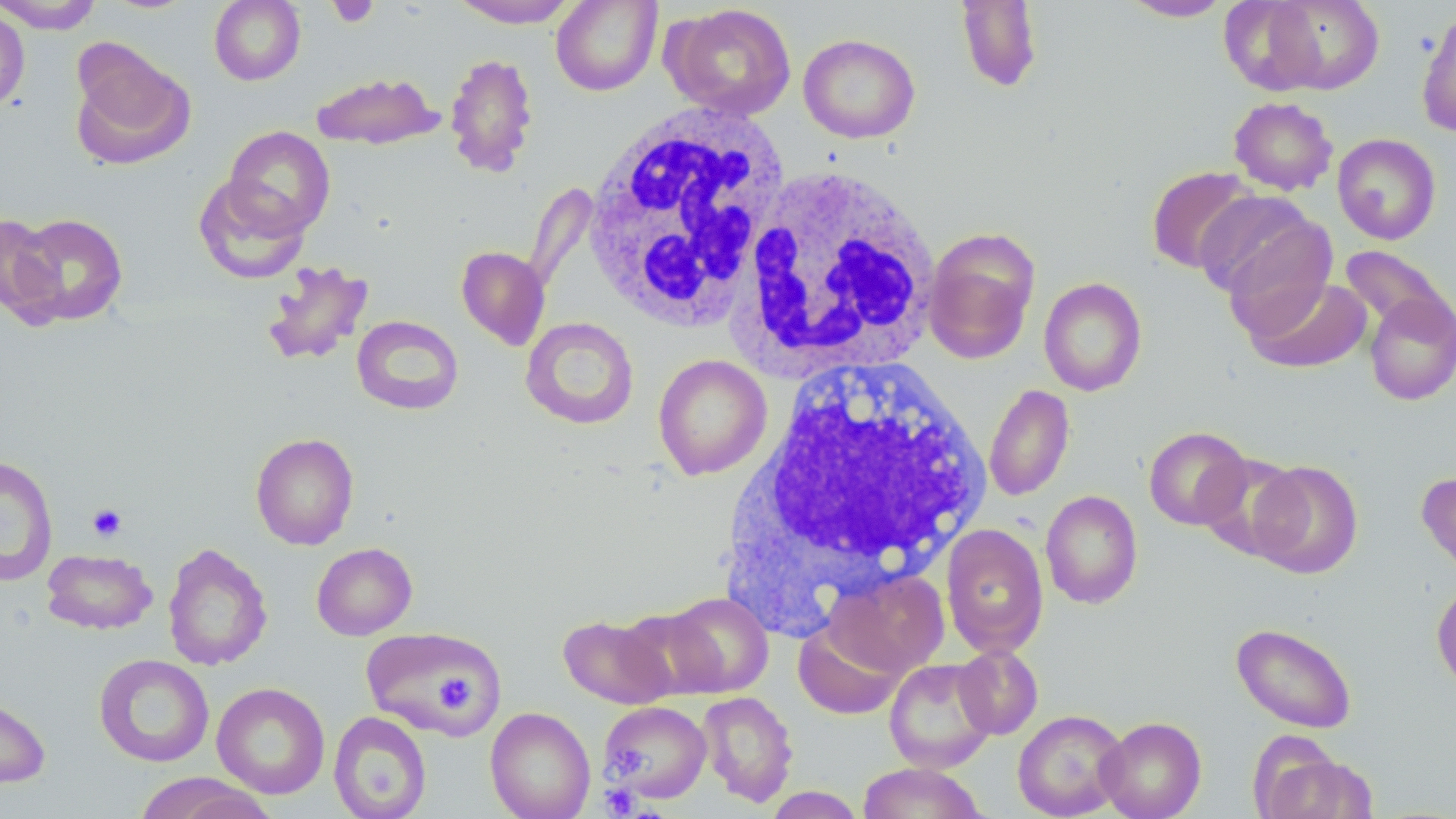
Summary:
  - Coordinate format: approximate bounding boxes as [x1, y1, x2, y2] in pixels
  - Uninfected red blood cell locations: [0, 0, 103, 34], [209, 0, 306, 86], [446, 0, 583, 28], [955, 0, 1043, 93], [1118, 0, 1234, 22], [551, 1, 662, 96], [1255, 1, 1385, 94], [6, 3, 76, 62], [664, 4, 797, 120], [0, 7, 30, 110], [1416, 10, 1456, 137], [798, 33, 921, 143], [69, 42, 194, 171], [444, 52, 539, 178], [311, 71, 443, 151], [1228, 97, 1338, 196], [224, 126, 334, 237], [1332, 133, 1441, 244], [1146, 166, 1259, 274], [194, 176, 311, 284], [1192, 190, 1327, 306], [11, 213, 129, 327], [0, 214, 65, 323], [923, 229, 1040, 364], [1338, 245, 1455, 345], [456, 246, 550, 350], [260, 259, 374, 367], [1038, 276, 1147, 397], [1245, 276, 1373, 373], [1363, 291, 1456, 406], [352, 315, 464, 415], [520, 317, 639, 430], [652, 353, 772, 480], [984, 383, 1075, 501], [1144, 426, 1252, 530], [250, 432, 359, 550], [1197, 451, 1305, 562], [0, 456, 58, 587], [1249, 460, 1364, 579], [1417, 470, 1456, 580], [1041, 489, 1143, 609], [940, 523, 1049, 657], [162, 542, 273, 671], [312, 542, 417, 640], [42, 549, 157, 634], [823, 568, 949, 677], [1432, 579, 1456, 690], [660, 592, 773, 698], [558, 612, 677, 709], [793, 620, 907, 719], [1231, 622, 1357, 734], [361, 627, 506, 736], [953, 644, 1044, 739], [94, 654, 214, 767], [883, 657, 998, 774], [212, 682, 330, 799], [698, 690, 798, 807], [0, 692, 51, 788], [600, 700, 711, 804], [485, 706, 596, 819], [1012, 709, 1129, 819], [328, 711, 432, 818], [1096, 716, 1206, 819], [1254, 745, 1377, 819], [856, 762, 988, 819], [131, 773, 277, 818], [763, 787, 866, 818]
  - Platelet locations: [327, 0, 379, 28], [87, 503, 127, 542], [434, 674, 473, 711], [612, 743, 645, 775], [601, 783, 640, 816]
  - White blood cell locations: [581, 103, 791, 332], [737, 163, 942, 376], [735, 354, 994, 599]
  - Slide-level diagnosis: negative for blood parasites
  - Modality: optical microscopy
  - Preparation: thin blood smear
  - Stain: May-Grünwald-Giemsa
  - Field of view: one of a larger specimen
  - Magnification: 1000x
  - Image size: 1456×819 pixels